Report the malaria status of this cell.
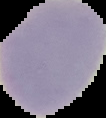
Parasitized.

{
  "image_size": "106×118 pixels",
  "image_type": "cell region segmented out of the field of view; surrounding area masked to black",
  "preparation": "thin blood film"
}